Outline each blood parasite and name the species.
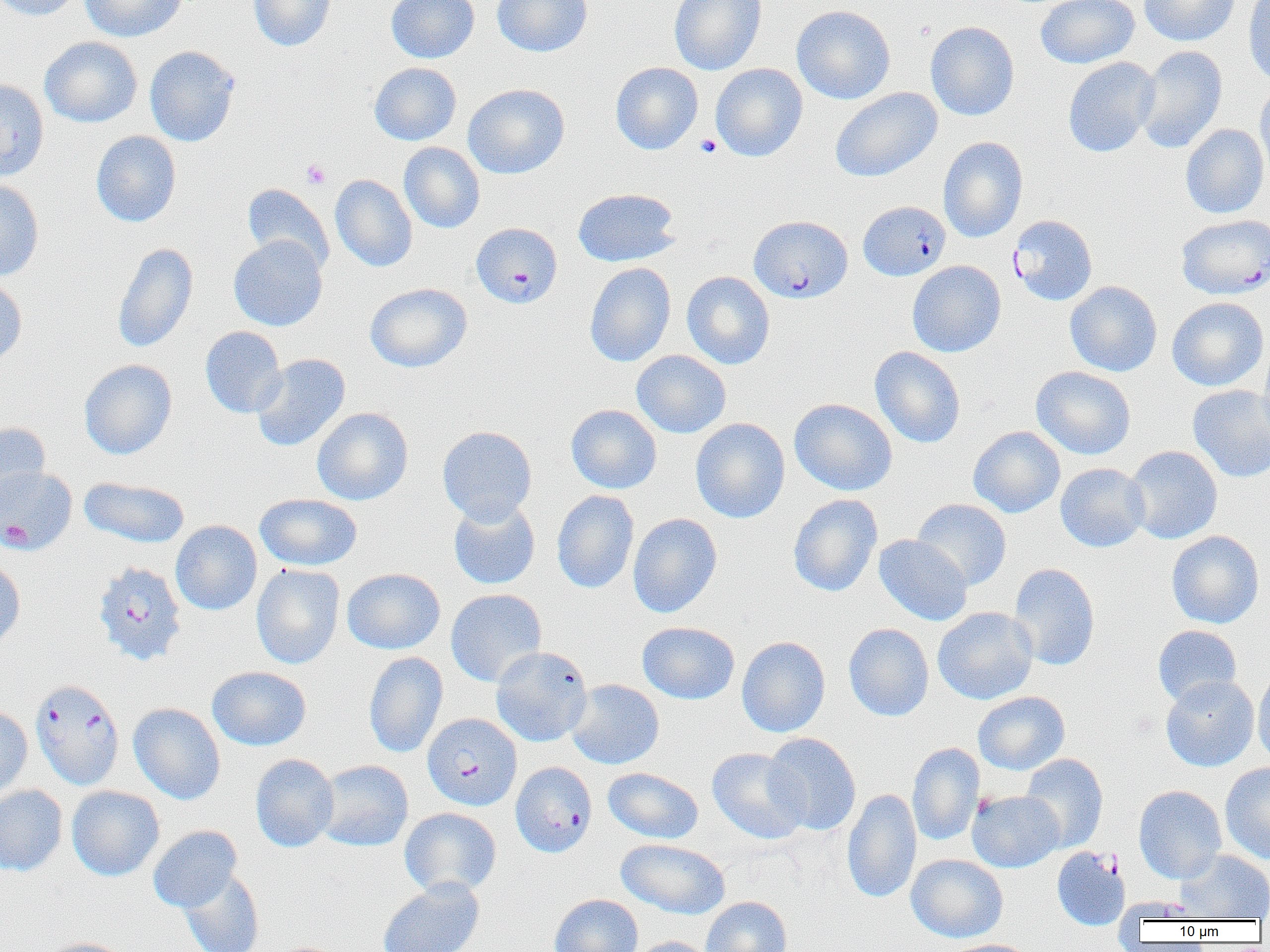
Approximate bounding boxes as (x1,y1)-(x2,y2) corner pairs in pixels.
Plasmodium falciparum-infected red blood cells: (857,201)-(951,281), (1008,214)-(1097,305), (749,215)-(853,303), (1177,215)-(1269,299), (472,222)-(562,308), (0,466)-(77,555), (92,561)-(188,666), (30,678)-(125,790), (423,713)-(521,811), (510,761)-(597,857).
No Plasmodium ovale, Plasmodium malariae, Plasmodium vivax, Babesia divergens, or Trypanosoma brucei observed.

slide-level diagnosis = Plasmodium falciparum
uninfected red blood cell locations = approximate bounding boxes as (x1,y1)-(x2,y2) corner pairs in pixels: (0,0)-(82,21), (80,0)-(187,42), (248,0)-(336,52), (386,0)-(479,63), (492,0)-(593,57), (669,0)-(766,75), (1035,0)-(1139,69), (1139,0)-(1239,46), (1243,0)-(1270,86), (791,5)-(896,104), (925,21)-(1019,121), (39,36)-(142,127), (144,45)-(240,147), (1135,45)-(1227,154), (1062,57)-(1160,157), (369,62)-(462,145), (610,62)-(703,154), (710,63)-(808,162), (0,79)-(49,182), (463,83)-(570,179), (1255,83)-(1270,183), (830,87)-(943,182), (1181,124)-(1269,219), (91,130)-(181,227), (938,137)-(1028,242), (399,142)-(485,233), (330,174)-(417,271), (0,179)-(44,281), (241,183)-(334,274), (572,188)-(680,267), (229,235)-(327,332), (112,242)-(198,353), (907,260)-(1006,357), (584,262)-(676,367), (682,271)-(775,369), (0,274)-(28,367), (1065,281)-(1162,377), (364,283)-(472,372), (1167,297)-(1269,391), (200,326)-(287,418), (1258,339)-(1270,447), (870,346)-(966,448), (631,350)-(731,438), (251,353)-(350,452), (79,359)-(177,459), (1031,366)-(1136,460), (1188,385)-(1270,482), (789,398)-(897,496), (566,404)-(662,494), (312,407)-(413,505), (691,417)-(790,523), (0,421)-(51,510), (437,425)-(537,525), (968,426)-(1065,518), (1124,445)-(1223,544), (1055,463)-(1150,552), (79,477)-(190,548), (552,490)-(639,593), (255,493)-(362,571), (788,493)-(883,597), (448,498)-(540,590), (911,498)-(1011,590), (628,513)-(723,618), (171,520)-(262,615), (1166,530)-(1264,629), (873,534)-(972,626), (0,557)-(26,651), (1008,562)-(1100,670), (251,564)-(345,669), (342,568)-(445,654), (446,589)-(547,687), (933,606)-(1038,704), (637,622)-(740,704), (844,623)-(934,721), (1152,625)-(1242,707), (736,636)-(830,737), (491,646)-(593,746), (363,652)-(448,758), (206,666)-(311,750), (1253,666)-(1270,769), (1160,675)-(1260,772), (565,679)-(664,769), (972,691)-(1070,775), (129,703)-(226,804), (0,706)-(32,802), (763,733)-(861,835), (907,742)-(984,847), (707,748)-(809,844), (250,753)-(339,852), (1020,753)-(1108,853), (314,759)-(413,852), (1220,761)-(1270,864), (603,767)-(704,844), (0,785)-(67,876), (66,785)-(165,881), (1134,785)-(1227,883), (842,788)-(921,904), (968,790)-(1064,872), (400,807)-(502,898), (148,825)-(242,912), (615,839)-(730,919), (1051,847)-(1130,931), (1176,850)-(1270,920), (906,854)-(1008,942), (179,868)-(265,952), (378,877)-(484,952), (549,894)-(643,952), (701,896)-(792,952), (629,936)-(716,952), (42,938)-(133,952), (943,939)-(1038,952)
field of view = one of a larger specimen
platelet locations = approximate bounding boxes as (x1,y1)-(x2,y2) corner pairs in pixels: (695,134)-(722,158), (301,159)-(331,189)
modality = optical microscopy
image size = 1270×952 pixels
magnification = 1000x
preparation = thin blood smear